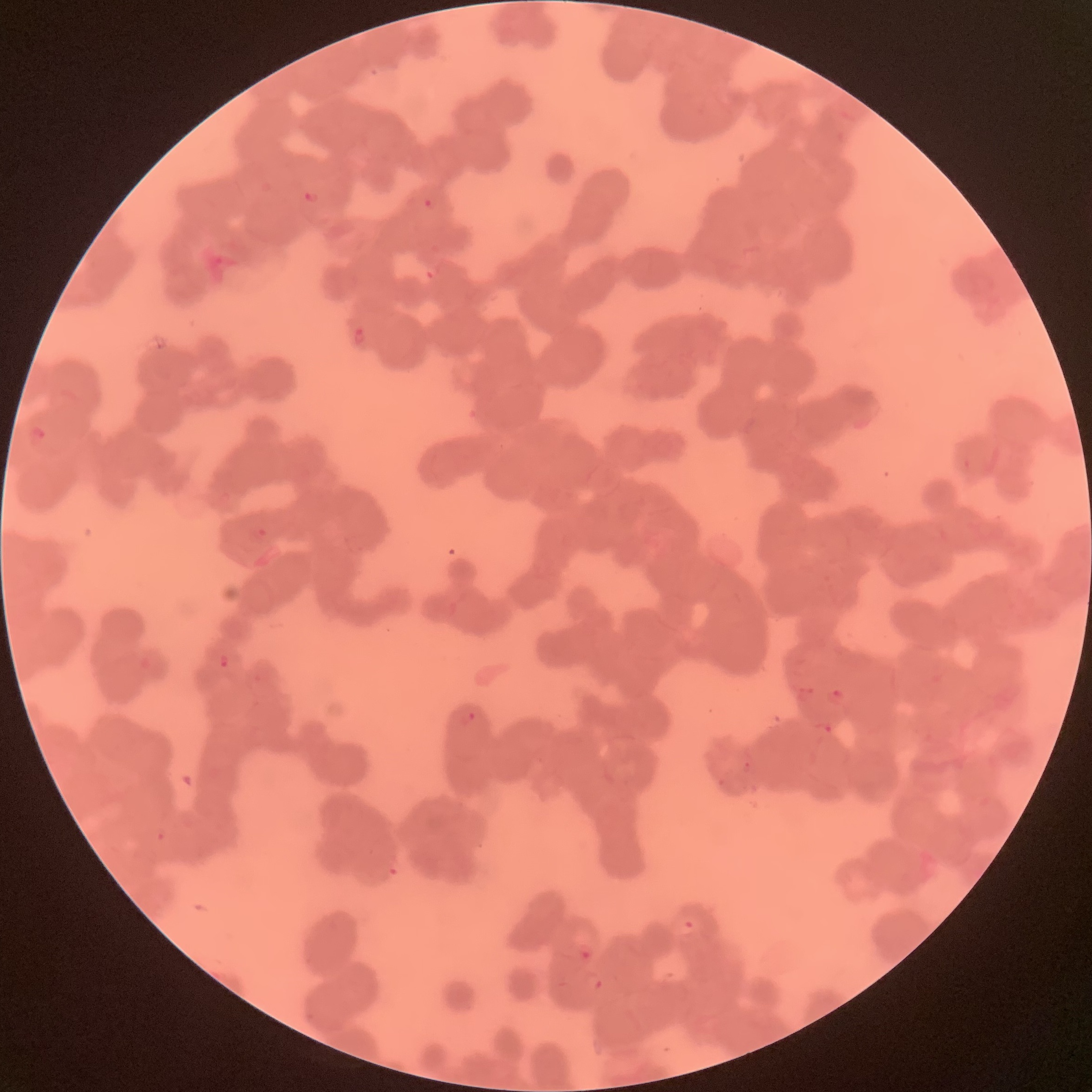 Approximate bounding boxes as named x1/y1/x2/y2 corners in pixels. Plasmodium parasite locations: (x1=302, y1=189, x2=320, y2=204), (x1=424, y1=197, x2=439, y2=211), (x1=351, y1=325, x2=366, y2=347), (x1=27, y1=425, x2=48, y2=447), (x1=218, y1=652, x2=232, y2=670), (x1=825, y1=685, x2=847, y2=708), (x1=456, y1=709, x2=476, y2=727), (x1=740, y1=760, x2=754, y2=774). The red blood cells show rouleaux formation. Thin blood smear. Image is 1092×1092 pixels. Optical microscopy.